Assess this cell for malaria.
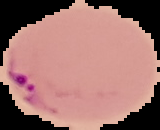

It is parasitized.

image_size: 160×130 pixels
image_type: segmented cell region with the area outside set to black
preparation: thin blood film